Name the blood parasite species.
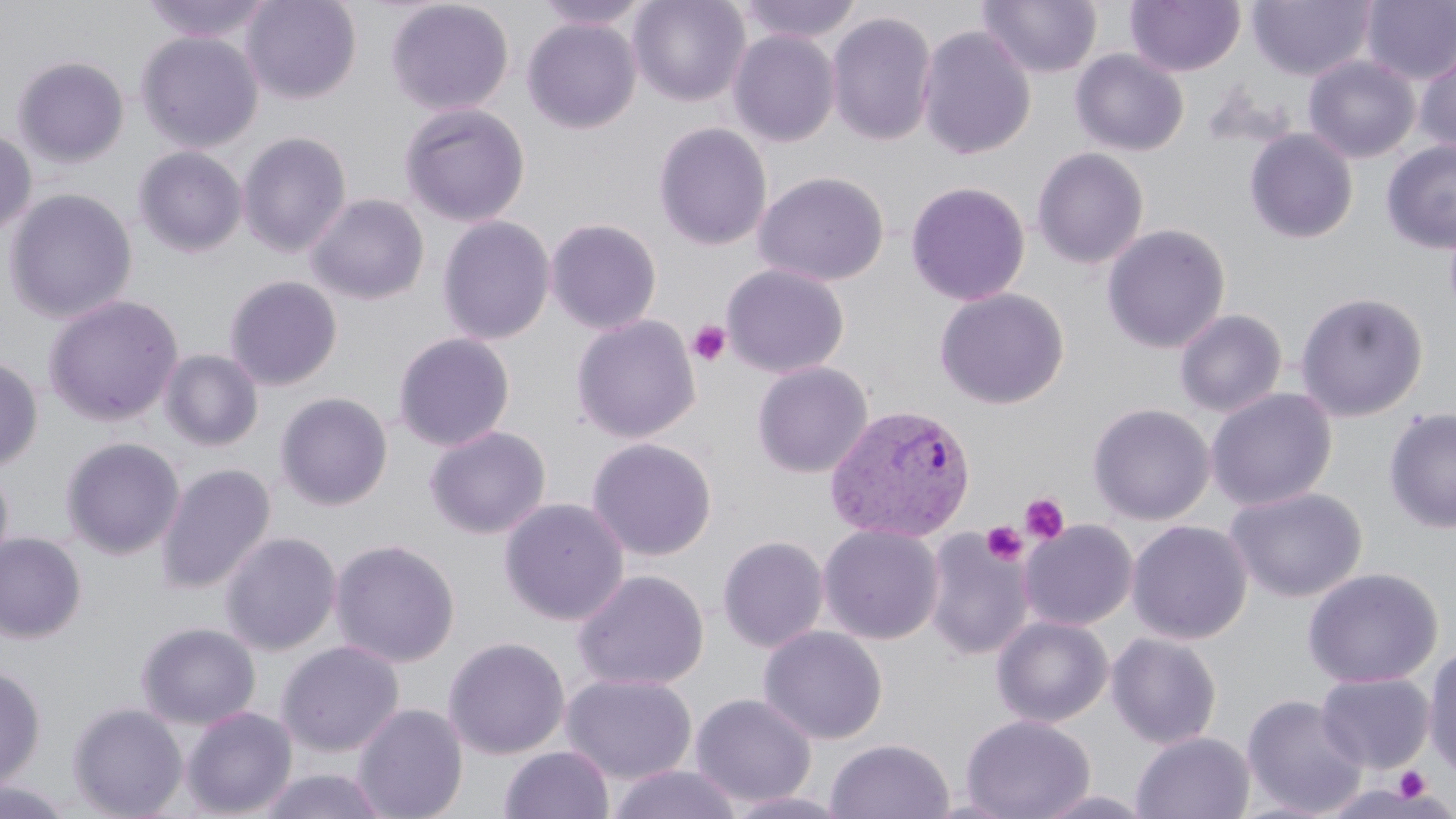

Plasmodium vivax.

Approximate bounding boxes as (x1,y1)-(x2,y2) corner pairs in pixels. Uninfected red blood cell locations: (139,0)-(274,43), (241,0)-(362,104), (533,0)-(652,31), (628,0)-(750,107), (737,0)-(862,45), (978,0)-(1102,79), (1248,0)-(1374,81), (386,1)-(514,116), (1125,1)-(1245,76), (1360,1)-(1456,85), (826,11)-(937,147), (523,18)-(642,134), (917,25)-(1036,160), (728,30)-(839,147), (137,32)-(263,153), (1414,43)-(1456,157), (1070,49)-(1189,157), (1303,55)-(1419,164), (13,57)-(129,167), (398,103)-(530,227), (654,122)-(773,252), (1244,128)-(1358,244), (0,130)-(36,239), (238,132)-(352,258), (1381,141)-(1456,254), (134,147)-(247,257), (1031,147)-(1149,269), (753,171)-(889,287), (905,181)-(1030,306), (4,188)-(138,324), (306,193)-(429,305), (437,215)-(555,346), (546,217)-(662,335), (1101,223)-(1231,354), (721,263)-(850,379), (225,275)-(342,391), (934,288)-(1069,409), (1294,291)-(1428,422), (43,294)-(184,427), (1174,308)-(1287,417), (570,314)-(701,444), (393,332)-(515,452), (160,349)-(263,451), (0,356)-(42,472), (751,362)-(874,478), (1205,387)-(1338,511), (276,392)-(392,510), (1087,403)-(1215,525), (1383,407)-(1456,534), (425,425)-(551,540), (62,437)-(184,559), (586,437)-(717,561), (0,459)-(14,579), (156,463)-(275,595), (1226,485)-(1366,603), (499,497)-(629,626), (1019,520)-(1137,631), (1127,520)-(1252,645), (818,524)-(943,645), (922,530)-(1035,661), (219,531)-(342,656), (0,533)-(86,643), (717,535)-(829,653), (330,538)-(460,668), (1303,567)-(1442,689), (572,568)-(709,692), (991,615)-(1113,728), (136,622)-(261,730), (758,626)-(888,745), (1106,632)-(1222,749), (443,636)-(570,759), (277,640)-(404,757), (1423,643)-(1456,783), (0,664)-(45,793), (1316,672)-(1435,773), (561,673)-(697,784), (690,693)-(817,808), (1241,693)-(1368,817), (68,703)-(188,819), (353,703)-(468,819), (181,706)-(297,818), (961,714)-(1095,819), (1131,731)-(1255,818), (825,738)-(955,819), (499,745)-(614,819), (607,763)-(743,819), (256,767)-(391,819), (0,779)-(77,819), (724,789)-(853,819), (1034,789)-(1156,819). Plasmodium vivax-infected red blood cell locations: (825,403)-(976,542). Platelet locations: (688,321)-(731,367), (1020,493)-(1069,545), (982,520)-(1027,565), (1393,767)-(1432,803). May-Grünwald-Giemsa stain. Thin blood film. Light microscopy. Image is 1456×819 pixels. Single field of view. 1000x magnification.